Name the parasite shown.
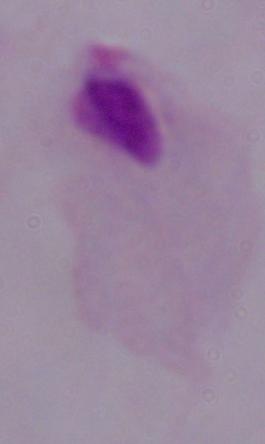
This is a trichomonad.

Summary:
  - Modality: micrograph
  - Magnification: 1000x